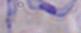

modality = micrograph
identification = trypanosome
magnification = 1000x